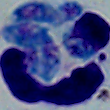

Photomicrograph. A leukocyte is seen. 1000x magnification.